Locate and identify every blood parasite.
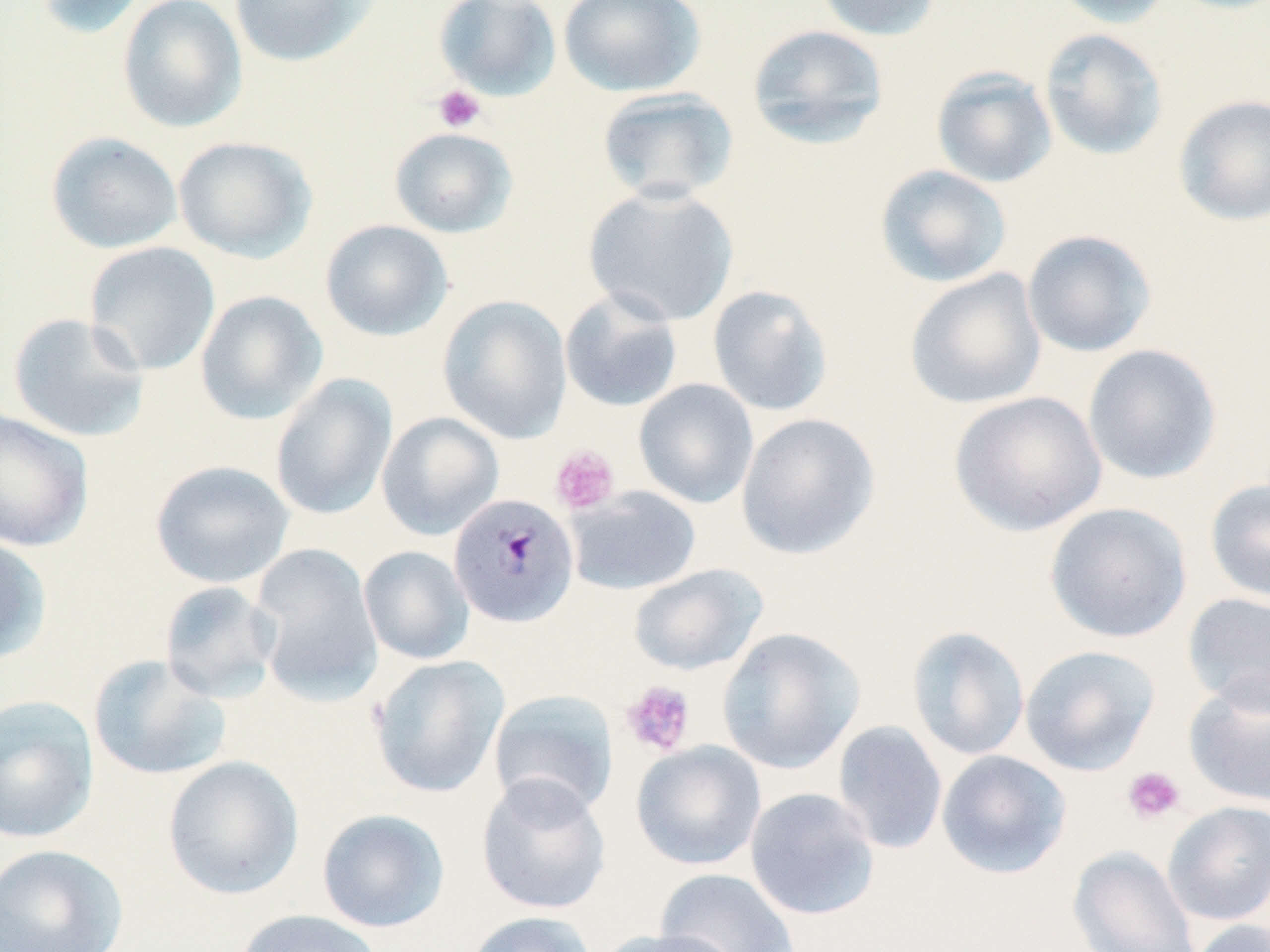
Approximate bounding boxes as (x1,y1)-(x2,y2) corner pairs in pixels.
Plasmodium malariae-infected red blood cells: (448,492)-(580,628).
No Plasmodium falciparum, Plasmodium ovale, Plasmodium vivax, Babesia divergens, or Trypanosoma brucei observed.

Uninfected red blood cell locations: (34,0)-(148,40), (117,0)-(247,133), (229,0)-(381,68), (433,0)-(563,103), (558,0)-(706,97), (812,0)-(943,41), (1049,0)-(1176,28), (746,23)-(890,149), (1039,27)-(1169,161), (931,67)-(1058,189), (596,86)-(740,205), (1172,94)-(1270,226), (388,126)-(518,238), (46,131)-(183,254), (172,136)-(318,263), (874,164)-(1013,288), (583,184)-(740,327), (319,219)-(453,341), (1021,229)-(1157,358), (84,241)-(220,375), (904,268)-(1047,410), (707,284)-(834,417), (559,287)-(683,413), (194,290)-(328,426), (436,295)-(573,444), (7,312)-(150,443), (1082,343)-(1223,485), (269,374)-(397,520), (633,379)-(759,509), (948,390)-(1107,536), (0,409)-(95,552), (376,411)-(505,541), (735,412)-(881,561), (149,460)-(295,588), (1204,477)-(1270,604), (565,486)-(702,595), (1044,502)-(1192,643), (0,532)-(52,666), (250,543)-(383,705), (359,545)-(474,664), (628,563)-(768,675), (158,580)-(281,703), (1182,591)-(1270,715), (906,625)-(1030,761), (716,627)-(865,774), (1020,644)-(1160,776), (88,654)-(232,782), (368,654)-(510,798), (1184,678)-(1270,807), (488,689)-(619,819), (0,694)-(99,844), (832,720)-(948,855), (631,740)-(767,871), (936,750)-(1072,879), (162,755)-(304,901), (476,774)-(612,915), (745,787)-(880,920), (1162,801)-(1270,926), (316,808)-(450,933), (1,844)-(130,952), (1068,845)-(1200,952), (655,868)-(799,951), (232,909)-(385,952), (463,910)-(598,952), (1187,919)-(1270,952), (599,928)-(745,952). Platelet locations: (432,85)-(486,133), (549,445)-(620,514), (620,680)-(696,756), (1121,765)-(1186,826). Slide-level diagnosis: Plasmodium malariae. Thin blood smear. Light microscopy. May-Grünwald-Giemsa stain. 1000x magnification. Single field of view. Image is 1270×952 pixels.